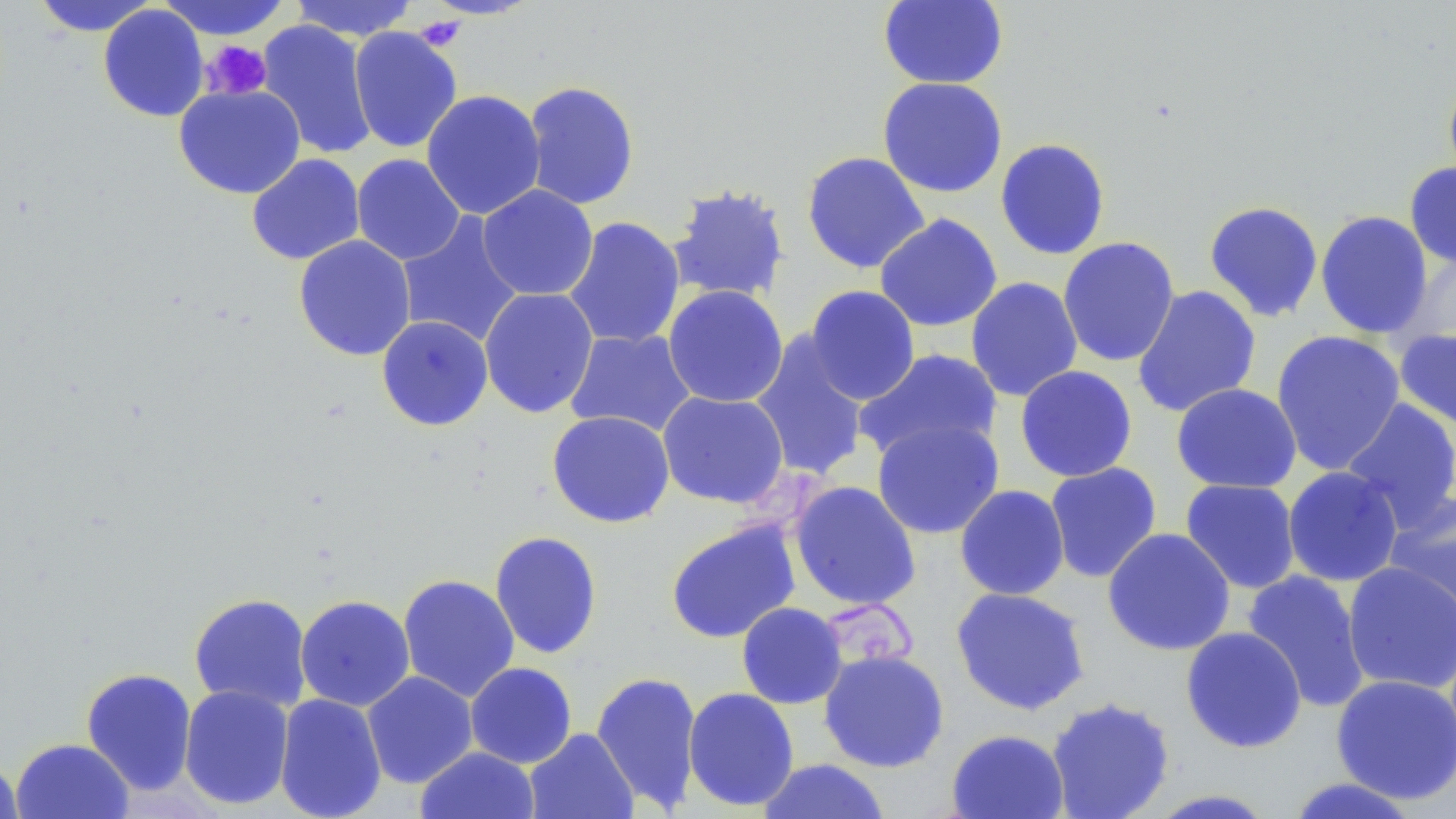
Approximate bounding boxes as named x1/y1/x2/y2 corners in pixels. Platelet locations: (x1=414, y1=15, x2=465, y2=51), (x1=200, y1=40, x2=272, y2=101), (x1=745, y1=471, x2=826, y2=530), (x1=828, y1=598, x2=918, y2=671). Uninfected red blood cell locations: (x1=157, y1=0, x2=292, y2=40), (x1=288, y1=0, x2=419, y2=41), (x1=878, y1=0, x2=1008, y2=90), (x1=31, y1=1, x2=159, y2=36), (x1=98, y1=4, x2=210, y2=122), (x1=256, y1=20, x2=377, y2=159), (x1=348, y1=26, x2=463, y2=154), (x1=1442, y1=72, x2=1456, y2=191), (x1=877, y1=77, x2=1008, y2=198), (x1=522, y1=80, x2=640, y2=210), (x1=173, y1=84, x2=306, y2=199), (x1=421, y1=89, x2=546, y2=220), (x1=994, y1=138, x2=1111, y2=260), (x1=801, y1=151, x2=930, y2=274), (x1=246, y1=153, x2=365, y2=265), (x1=352, y1=154, x2=466, y2=265), (x1=1404, y1=161, x2=1456, y2=270), (x1=666, y1=184, x2=791, y2=304), (x1=477, y1=185, x2=598, y2=301), (x1=1203, y1=200, x2=1324, y2=323), (x1=1315, y1=210, x2=1433, y2=339), (x1=874, y1=213, x2=1003, y2=332), (x1=396, y1=214, x2=525, y2=348), (x1=563, y1=216, x2=686, y2=350), (x1=293, y1=235, x2=416, y2=361), (x1=1058, y1=236, x2=1180, y2=367), (x1=1405, y1=249, x2=1456, y2=351), (x1=965, y1=276, x2=1083, y2=402), (x1=662, y1=285, x2=789, y2=408), (x1=804, y1=285, x2=920, y2=405), (x1=1132, y1=285, x2=1262, y2=417), (x1=479, y1=287, x2=599, y2=419), (x1=377, y1=315, x2=493, y2=431), (x1=564, y1=328, x2=697, y2=438), (x1=1394, y1=328, x2=1456, y2=434), (x1=1271, y1=329, x2=1406, y2=476), (x1=750, y1=331, x2=871, y2=482), (x1=855, y1=347, x2=1004, y2=463), (x1=1015, y1=365, x2=1138, y2=482), (x1=1171, y1=383, x2=1302, y2=494), (x1=657, y1=391, x2=789, y2=508), (x1=1340, y1=398, x2=1456, y2=532), (x1=547, y1=410, x2=675, y2=528), (x1=871, y1=418, x2=1005, y2=539), (x1=1044, y1=462, x2=1162, y2=583), (x1=1282, y1=466, x2=1404, y2=587), (x1=1180, y1=478, x2=1301, y2=594), (x1=788, y1=480, x2=922, y2=611), (x1=955, y1=484, x2=1070, y2=600), (x1=1383, y1=492, x2=1456, y2=626), (x1=665, y1=519, x2=801, y2=644), (x1=1102, y1=527, x2=1236, y2=656), (x1=489, y1=530, x2=603, y2=659), (x1=1341, y1=561, x2=1456, y2=695), (x1=1241, y1=570, x2=1371, y2=713), (x1=398, y1=574, x2=520, y2=702), (x1=951, y1=586, x2=1091, y2=716), (x1=189, y1=593, x2=312, y2=712), (x1=295, y1=595, x2=415, y2=711), (x1=736, y1=602, x2=847, y2=709), (x1=1180, y1=625, x2=1307, y2=753), (x1=818, y1=649, x2=949, y2=773), (x1=465, y1=662, x2=577, y2=768), (x1=81, y1=667, x2=198, y2=795), (x1=590, y1=670, x2=703, y2=813), (x1=362, y1=671, x2=478, y2=788), (x1=1331, y1=674, x2=1456, y2=804), (x1=178, y1=684, x2=294, y2=810), (x1=682, y1=687, x2=800, y2=812), (x1=274, y1=693, x2=387, y2=819), (x1=1046, y1=696, x2=1175, y2=819), (x1=524, y1=728, x2=638, y2=819), (x1=946, y1=728, x2=1070, y2=819), (x1=10, y1=738, x2=134, y2=819), (x1=415, y1=746, x2=540, y2=819), (x1=0, y1=755, x2=24, y2=819), (x1=756, y1=758, x2=891, y2=818), (x1=1284, y1=777, x2=1423, y2=818), (x1=1145, y1=789, x2=1280, y2=818). Slide-level diagnosis: no evidence of blood parasites. Optical microscopy. Captured at 1000x magnification. Image is 1456×819 pixels. May-Grünwald-Giemsa-stained preparation. Single field of view. Thin blood smear.